Locate every uninfected red blood cell.
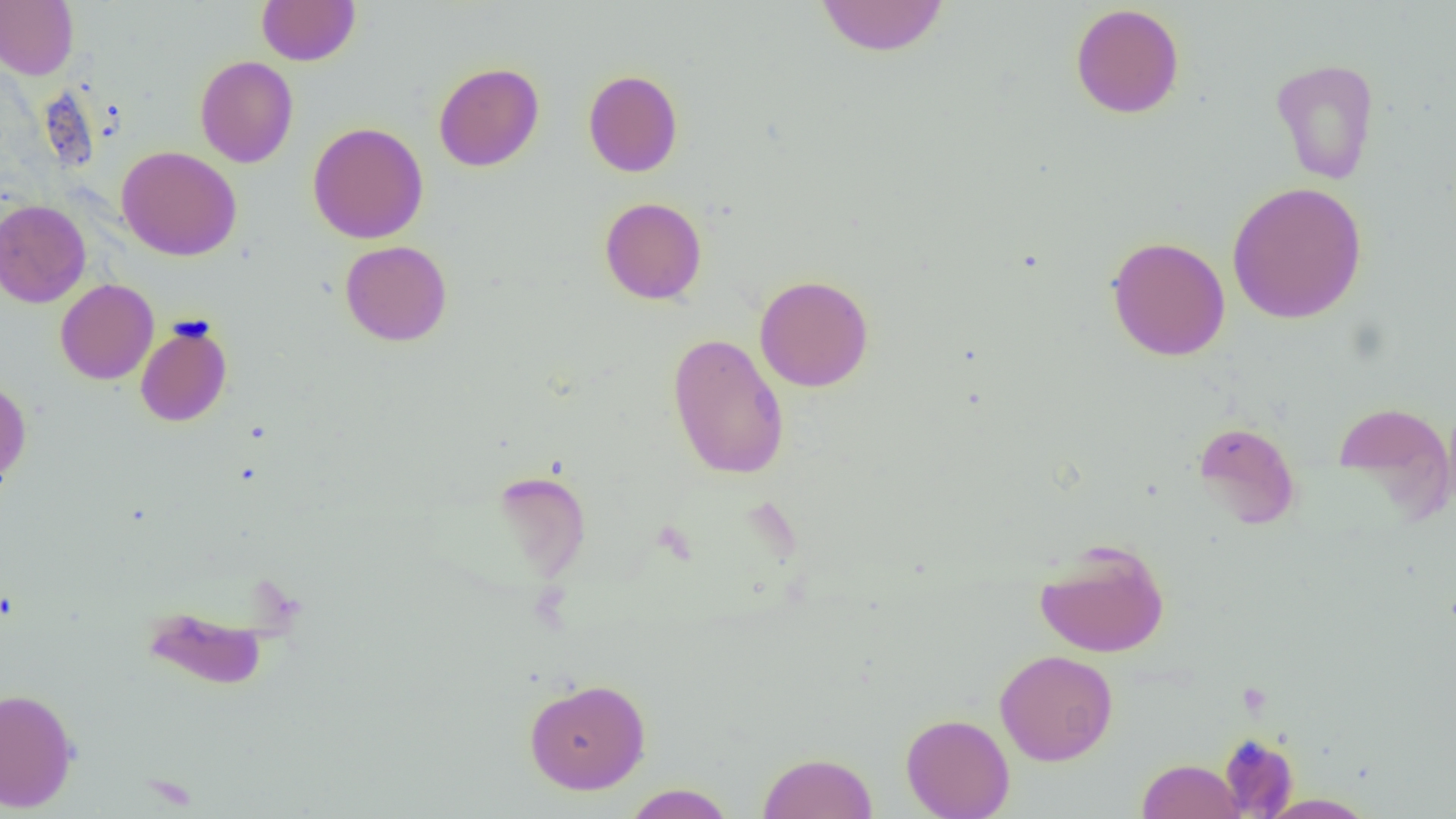
Approximate bounding boxes as [x1, y1, x2, y2] in pixels.
Uninfected red blood cells: [0, 0, 79, 79], [256, 0, 360, 66], [814, 0, 949, 57], [1070, 3, 1185, 119], [195, 56, 299, 168], [1270, 58, 1380, 185], [434, 62, 544, 171], [583, 69, 683, 177], [307, 122, 429, 244], [116, 146, 242, 261], [1227, 181, 1367, 324], [599, 197, 707, 304], [0, 199, 91, 307], [1106, 236, 1230, 361], [340, 240, 452, 346], [755, 274, 874, 392], [55, 279, 158, 385], [135, 319, 233, 427], [667, 332, 789, 480], [0, 380, 31, 487], [1443, 396, 1456, 518], [1333, 402, 1454, 513], [1193, 421, 1301, 529], [491, 470, 591, 582], [1034, 539, 1170, 658], [140, 604, 272, 691], [995, 649, 1118, 766], [524, 677, 651, 794], [0, 688, 79, 812], [901, 712, 1014, 819], [1218, 733, 1299, 817], [758, 751, 877, 819], [1136, 758, 1246, 819], [623, 783, 736, 818], [1259, 793, 1377, 818].

slide-level diagnosis = negative for blood parasites
field of view = single
image size = 1456×819 pixels
magnification = 1000x
preparation = thin blood film
modality = optical microscopy